Report the malaria status of this cell.
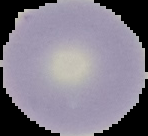

It is uninfected.

Summary:
  - Image type: cell region segmented out of the field of view; surrounding area masked to black
  - Preparation: thin blood film
  - Image size: 148×136 pixels